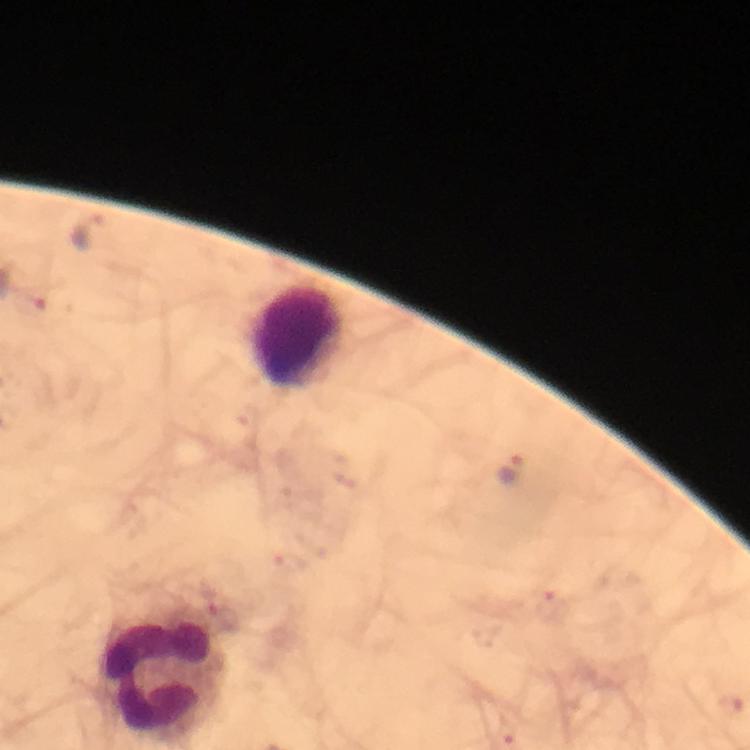
Approximate object centers, in pixels from the top-left corner. Leukocyte locations: (x=299, y=336), (x=158, y=675). Plasmodium parasite locations: (x=90, y=231), (x=34, y=304), (x=513, y=469), (x=550, y=604). Giemsa stain. From a malaria diagnostic workup. 100x magnification. Immersion oil applied. A crop from one field of view. Image is 750×750 pixels. Photographed with a smartphone mounted on the microscope. Thick smear.